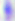

Toxoplasma gondii is seen. Photomicrograph. Captured at 400x magnification.